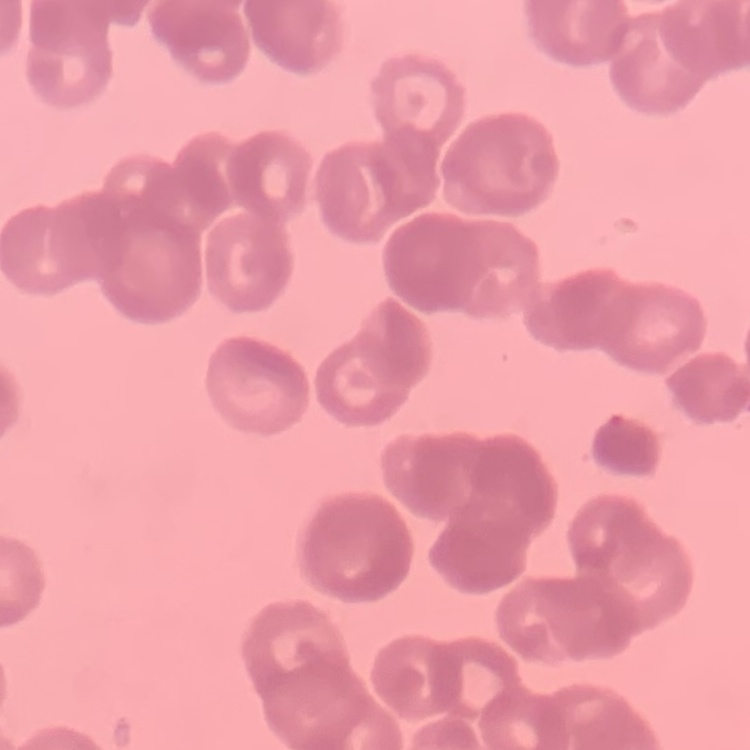

Summary:
  - Red blood cell morphology: rouleaux formation
  - Image type: one tile cut from a larger photomicrograph
  - Stain: Field's or Giemsa
  - Preparation: thin blood film